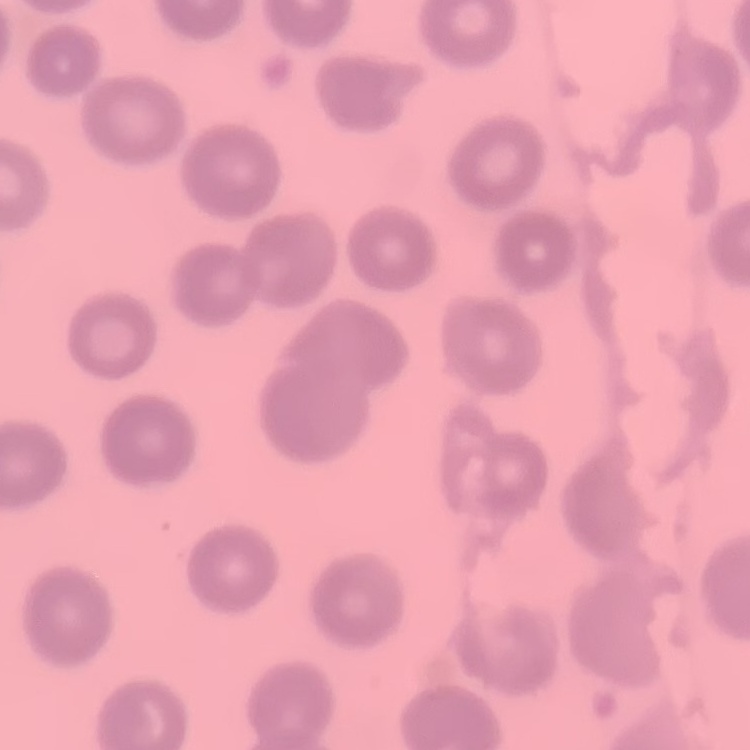

red blood cell morphology = no rouleaux formation
image type = square crop of a larger photomicrograph
stain = Field's or Giemsa
preparation = thin blood film